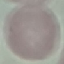

Summary:
  - Malaria status: uninfected
  - Preparation: thin blood smear
  - Image type: cell patch, automatically extracted from a larger field of view and resized to 64 × 64 pixels
  - Stain: Giemsa
  - Capture: smartphone camera at the microscope eyepiece